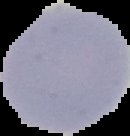
result: no malaria parasites seen
preparation: thin blood smear
image_size: 130×136 pixels
image_type: segmented cell region with the area outside set to black